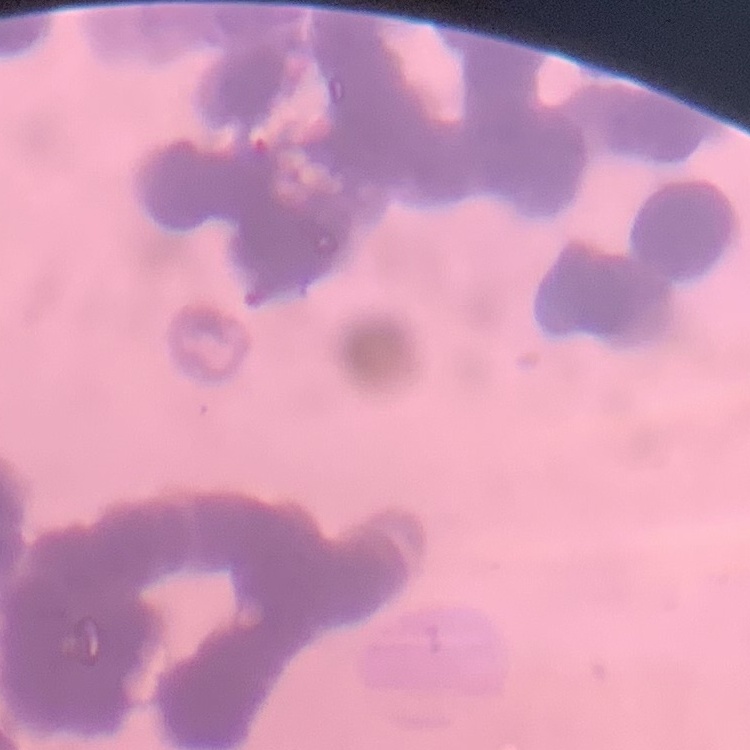
Summary:
  - Erythrocyte morphology: rouleaux formation
  - Image type: one tile cut from a larger photomicrograph
  - Preparation: thin peripheral smear
  - Stain: Field's or Giemsa